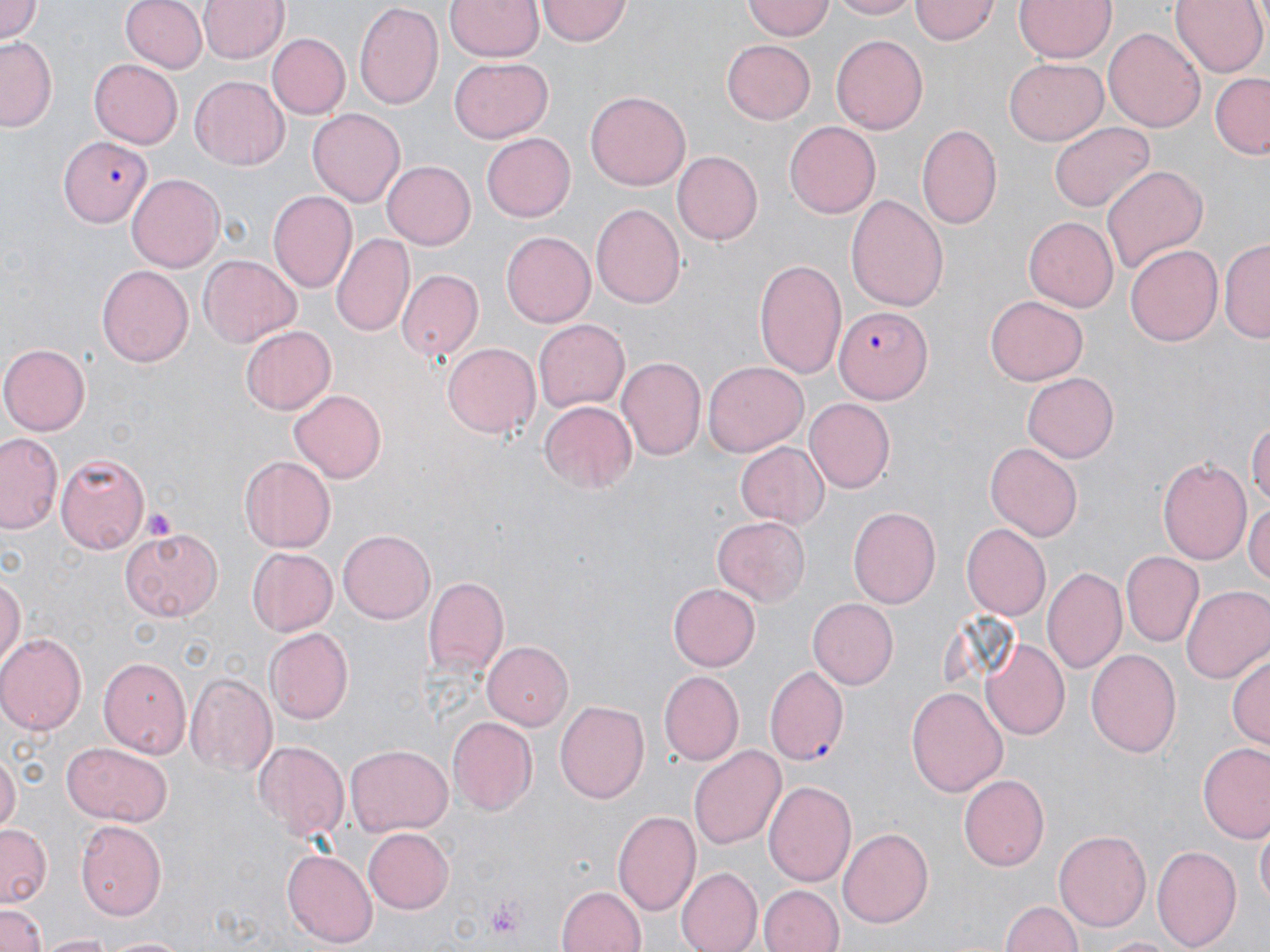
Approximate bounding boxes as named x1/y1/x2/y2 corners in pixels. Uninfected red blood cell locations: (x1=0, y1=0, x2=44, y2=44), (x1=120, y1=0, x2=208, y2=75), (x1=198, y1=0, x2=286, y2=65), (x1=355, y1=0, x2=445, y2=111), (x1=446, y1=0, x2=543, y2=63), (x1=743, y1=0, x2=832, y2=40), (x1=826, y1=0, x2=918, y2=19), (x1=912, y1=0, x2=999, y2=44), (x1=1015, y1=0, x2=1114, y2=63), (x1=1170, y1=0, x2=1265, y2=78), (x1=538, y1=1, x2=631, y2=46), (x1=1103, y1=25, x2=1204, y2=131), (x1=266, y1=32, x2=349, y2=119), (x1=830, y1=34, x2=929, y2=136), (x1=1, y1=37, x2=59, y2=133), (x1=722, y1=41, x2=816, y2=123), (x1=1004, y1=57, x2=1106, y2=144), (x1=450, y1=58, x2=552, y2=143), (x1=88, y1=59, x2=182, y2=149), (x1=1210, y1=75, x2=1270, y2=158), (x1=190, y1=76, x2=290, y2=170), (x1=585, y1=90, x2=692, y2=191), (x1=308, y1=107, x2=404, y2=204), (x1=784, y1=121, x2=881, y2=219), (x1=1050, y1=122, x2=1154, y2=213), (x1=915, y1=123, x2=1002, y2=231), (x1=482, y1=132, x2=576, y2=222), (x1=673, y1=151, x2=762, y2=246), (x1=382, y1=162, x2=475, y2=248), (x1=1101, y1=166, x2=1207, y2=275), (x1=127, y1=175, x2=225, y2=272), (x1=267, y1=190, x2=358, y2=294), (x1=847, y1=194, x2=948, y2=312), (x1=591, y1=203, x2=687, y2=307), (x1=1024, y1=217, x2=1118, y2=313), (x1=331, y1=232, x2=415, y2=338), (x1=500, y1=232, x2=594, y2=328), (x1=1221, y1=239, x2=1270, y2=343), (x1=1124, y1=244, x2=1225, y2=347), (x1=198, y1=253, x2=299, y2=346), (x1=755, y1=259, x2=845, y2=380), (x1=97, y1=265, x2=195, y2=367), (x1=396, y1=271, x2=483, y2=359), (x1=987, y1=294, x2=1087, y2=384), (x1=533, y1=318, x2=628, y2=413), (x1=239, y1=326, x2=337, y2=416), (x1=0, y1=341, x2=90, y2=436), (x1=441, y1=341, x2=539, y2=439), (x1=615, y1=358, x2=705, y2=463), (x1=703, y1=361, x2=808, y2=457), (x1=1021, y1=372, x2=1120, y2=465), (x1=288, y1=389, x2=387, y2=483), (x1=803, y1=398, x2=894, y2=491), (x1=540, y1=399, x2=638, y2=493), (x1=1249, y1=417, x2=1270, y2=510), (x1=1, y1=432, x2=64, y2=534), (x1=736, y1=442, x2=829, y2=529), (x1=986, y1=443, x2=1082, y2=541), (x1=56, y1=452, x2=148, y2=552), (x1=1158, y1=455, x2=1254, y2=564), (x1=239, y1=457, x2=334, y2=552), (x1=1244, y1=500, x2=1270, y2=589), (x1=848, y1=506, x2=940, y2=608), (x1=711, y1=517, x2=811, y2=607), (x1=962, y1=524, x2=1050, y2=620), (x1=122, y1=528, x2=223, y2=622), (x1=339, y1=529, x2=437, y2=624), (x1=247, y1=549, x2=336, y2=635), (x1=1123, y1=552, x2=1203, y2=648), (x1=1043, y1=564, x2=1127, y2=674), (x1=1, y1=566, x2=27, y2=673), (x1=424, y1=578, x2=508, y2=681), (x1=670, y1=582, x2=760, y2=671), (x1=1181, y1=583, x2=1270, y2=683), (x1=806, y1=598, x2=899, y2=690), (x1=265, y1=627, x2=354, y2=726), (x1=0, y1=633, x2=85, y2=733), (x1=979, y1=639, x2=1068, y2=741), (x1=483, y1=642, x2=575, y2=730), (x1=1087, y1=648, x2=1181, y2=758), (x1=1228, y1=648, x2=1269, y2=751), (x1=98, y1=656, x2=192, y2=756), (x1=765, y1=667, x2=848, y2=764), (x1=660, y1=671, x2=743, y2=766), (x1=185, y1=674, x2=276, y2=778), (x1=907, y1=685, x2=1009, y2=800), (x1=555, y1=700, x2=651, y2=803), (x1=448, y1=717, x2=538, y2=816), (x1=253, y1=739, x2=349, y2=841), (x1=1198, y1=741, x2=1270, y2=842), (x1=63, y1=742, x2=172, y2=824), (x1=346, y1=745, x2=454, y2=837), (x1=689, y1=745, x2=786, y2=853), (x1=0, y1=750, x2=19, y2=836), (x1=960, y1=773, x2=1050, y2=871), (x1=766, y1=779, x2=857, y2=888), (x1=614, y1=809, x2=702, y2=919), (x1=76, y1=819, x2=166, y2=921), (x1=0, y1=824, x2=51, y2=906), (x1=838, y1=826, x2=933, y2=928), (x1=362, y1=827, x2=453, y2=914), (x1=1256, y1=828, x2=1269, y2=909), (x1=1056, y1=830, x2=1151, y2=933), (x1=1152, y1=843, x2=1242, y2=952), (x1=281, y1=846, x2=376, y2=947), (x1=678, y1=867, x2=762, y2=952), (x1=556, y1=883, x2=648, y2=952), (x1=758, y1=885, x2=843, y2=952), (x1=1001, y1=898, x2=1081, y2=952), (x1=2, y1=906, x2=45, y2=952), (x1=41, y1=933, x2=114, y2=952), (x1=101, y1=934, x2=187, y2=951), (x1=1092, y1=935, x2=1185, y2=952). Plasmodium falciparum-infected red blood cell locations: (x1=57, y1=135, x2=154, y2=228), (x1=835, y1=307, x2=930, y2=404). Platelet locations: (x1=142, y1=507, x2=182, y2=542), (x1=483, y1=894, x2=529, y2=941). Slide-level diagnosis: Plasmodium falciparum. Image is 1270×952 pixels. Light microscopy. 1000x magnification. Thin blood film. May-Grünwald-Giemsa-stained preparation. Single field of view.